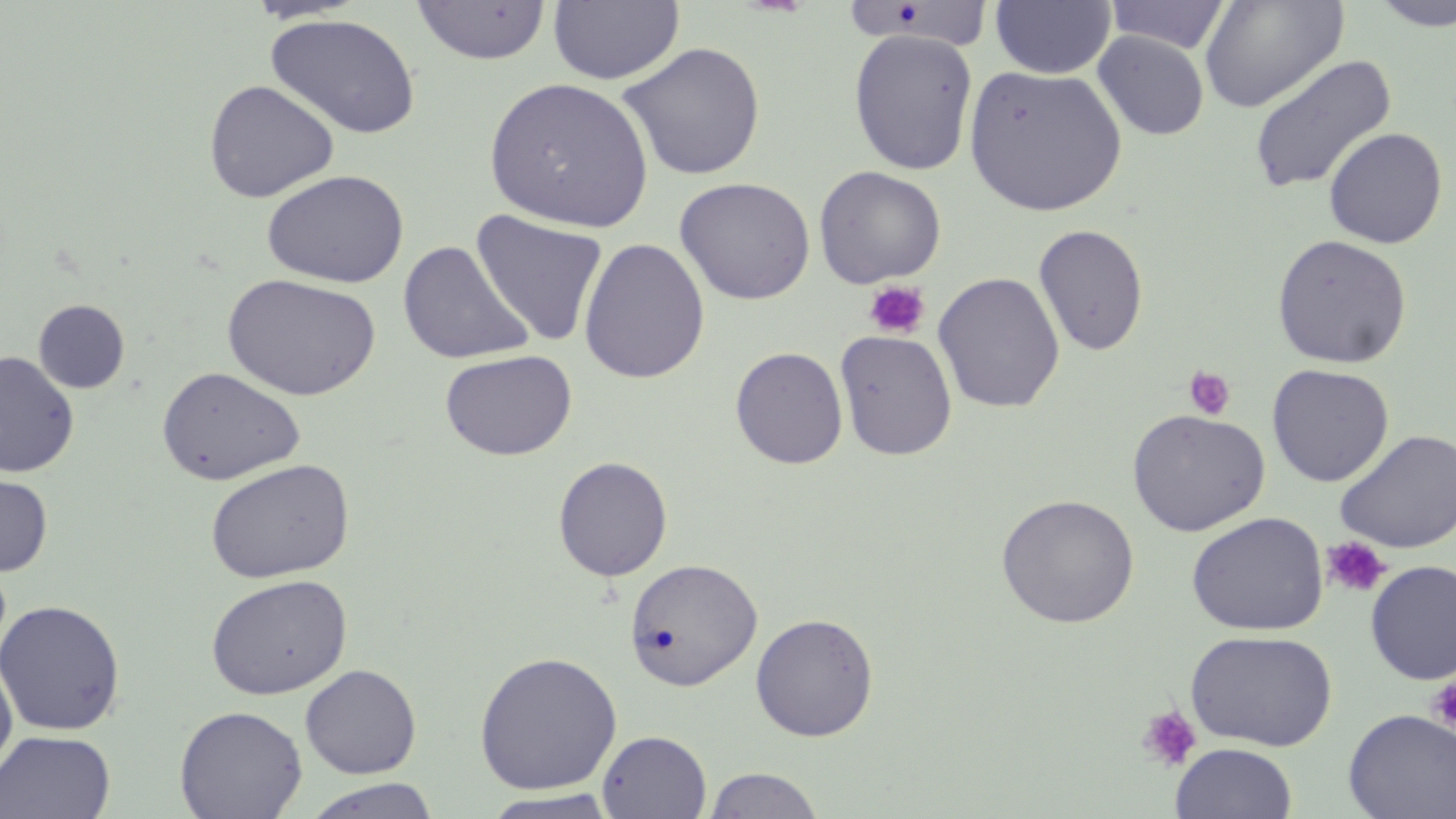

slide_level_diagnosis: negative for blood parasites
stain: May-Grünwald-Giemsa
image_size: 1456×819 pixels
field_of_view: one of a larger specimen
modality: light microscopy
preparation: thin blood film
platelet_locations: 'approximate bounding boxes as (x1,y1)-(x2,y2) corner pairs in pixels: (863,280)-(931,340), (1183,365)-(1237,421), (1321,536)-(1393,598), (1426,676)-(1456,732), (1136,705)-(1202,772)'
uninfected_red_blood_cell_locations: 'approximate bounding boxes as (x1,y1)-(x2,y2) corner pairs in pixels: (411,0)-(553,65), (548,0)-(685,85), (846,0)-(995,54), (990,0)-(1116,79), (1104,0)-(1233,55), (1199,0)-(1348,114), (1369,0)-(1456,31), (264,13)-(422,140), (848,28)-(978,175), (1092,30)-(1209,141), (617,41)-(766,181), (1247,54)-(1398,194), (963,64)-(1128,217), (483,76)-(655,233), (202,78)-(340,202), (1323,126)-(1448,249), (813,165)-(946,288), (260,169)-(409,288), (674,177)-(816,305), (470,209)-(609,347), (1032,223)-(1149,356), (1271,234)-(1413,369), (578,237)-(711,385), (398,240)-(533,364), (933,271)-(1066,413), (222,273)-(381,401), (33,299)-(130,393), (834,329)-(958,461), (730,346)-(848,469), (439,349)-(577,461), (0,351)-(79,476), (1266,363)-(1394,487), (156,366)-(305,485), (1127,408)-(1270,537), (1335,429)-(1456,554), (553,455)-(673,581), (205,458)-(355,583), (0,469)-(53,577), (996,493)-(1140,629), (1186,511)-(1329,636), (623,557)-(762,691), (1364,560)-(1456,685), (205,573)-(352,700), (0,599)-(126,736), (750,612)-(879,741), (1184,629)-(1338,750), (474,650)-(623,796), (0,654)-(17,785), (300,663)-(421,779), (174,705)-(307,819), (1343,708)-(1456,819), (0,730)-(115,818), (598,730)-(712,819), (1170,742)-(1298,819), (703,766)-(824,818), (302,778)-(440,818), (481,790)-(621,818)'
magnification: 1000x